Identify the parasite.
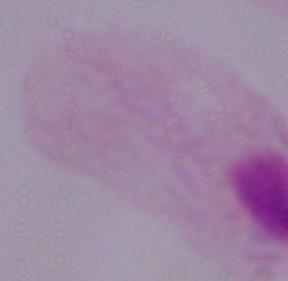

A trichomonad.

Captured at 1000x magnification. Micrograph.